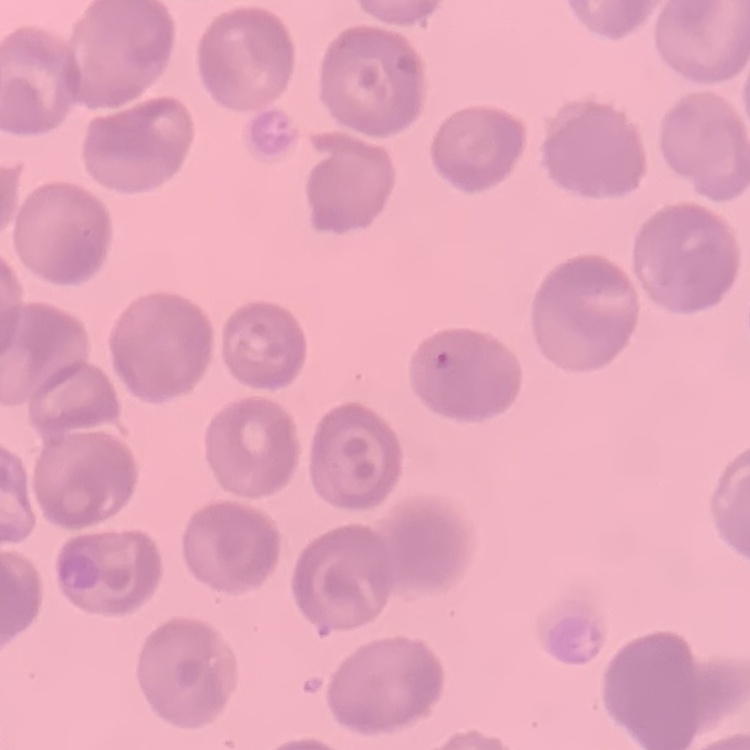

The erythrocytes exhibit no rouleaux formation. Stained with either Field's or Giemsa. Thin peripheral smear. Square crop of a larger photomicrograph.